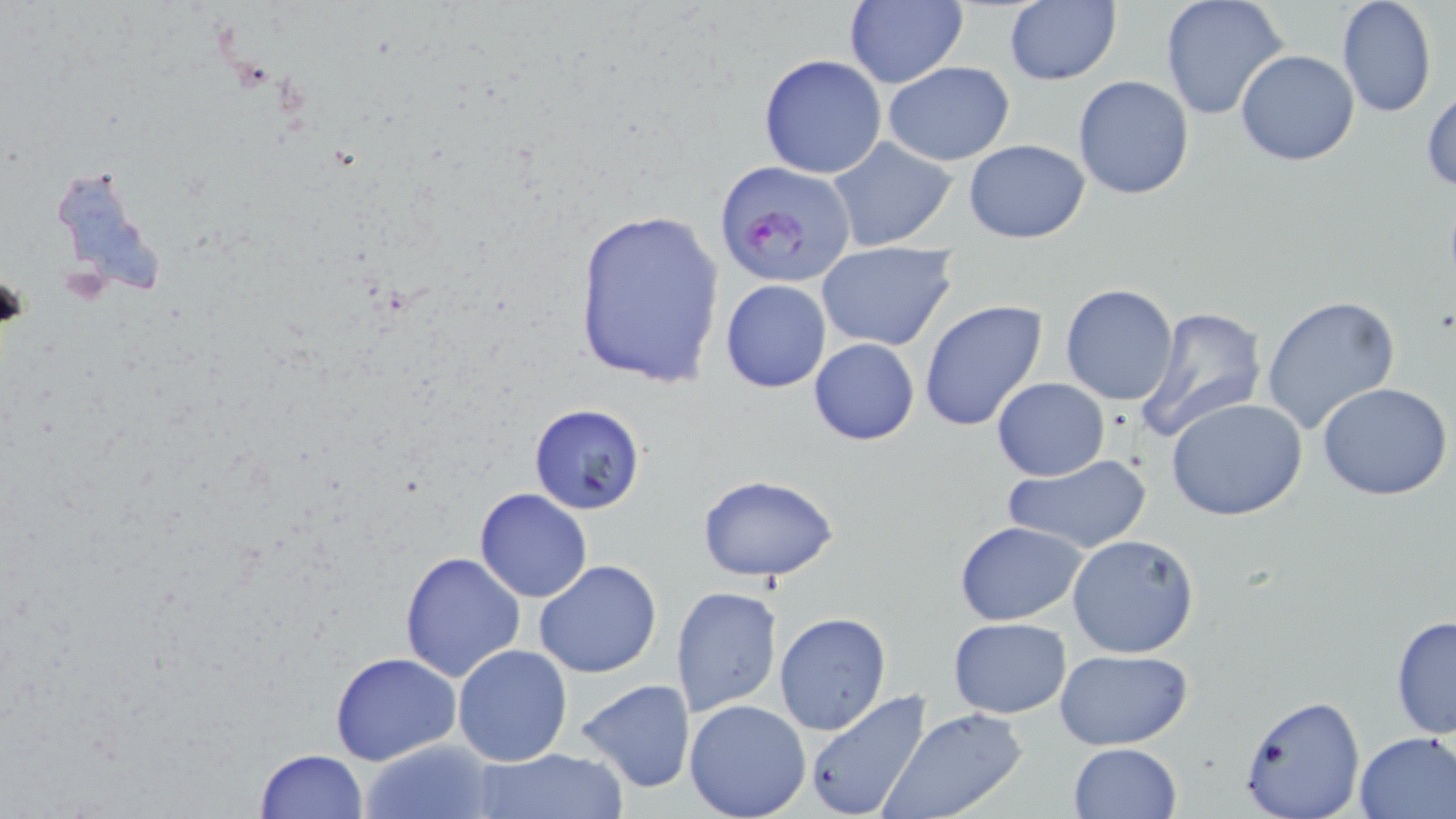 Approximate bounding boxes as [x1, y1, x2, y2] in pixels. Plasmodium falciparum-infected red blood cell locations: [717, 160, 857, 290]. Uninfected red blood cell locations: [1159, 0, 1291, 121], [1336, 0, 1438, 119], [841, 1, 968, 90], [1003, 2, 1120, 85], [1235, 48, 1360, 166], [758, 55, 887, 179], [883, 60, 1015, 165], [1072, 75, 1194, 200], [1422, 85, 1455, 193], [828, 137, 958, 250], [962, 138, 1091, 243], [49, 161, 174, 303], [571, 208, 726, 389], [816, 242, 958, 351], [720, 278, 831, 392], [1060, 283, 1179, 405], [1262, 296, 1401, 437], [919, 299, 1049, 433], [1134, 306, 1269, 439], [808, 338, 921, 446], [992, 377, 1109, 481], [1317, 382, 1452, 501], [1166, 397, 1309, 522], [528, 403, 647, 516], [1002, 454, 1153, 554], [694, 473, 841, 583], [474, 488, 594, 602], [954, 520, 1087, 626], [1067, 533, 1199, 658], [399, 551, 526, 682], [535, 560, 660, 678], [671, 585, 782, 719], [773, 611, 892, 736], [1389, 613, 1455, 741], [948, 617, 1072, 718], [453, 644, 573, 766], [1053, 648, 1193, 749], [330, 651, 462, 765], [574, 678, 697, 793], [802, 690, 934, 819], [1236, 693, 1366, 819], [682, 699, 812, 819], [881, 708, 1031, 819], [1352, 730, 1456, 817], [359, 738, 493, 819], [1067, 743, 1183, 819], [470, 746, 628, 819], [253, 748, 368, 819]. Slide-level diagnosis: Plasmodium falciparum. May-Grünwald-Giemsa stain. One field of a larger specimen. 1000x magnification. Thin blood film. Image is 1456×819 pixels. Optical microscopy.